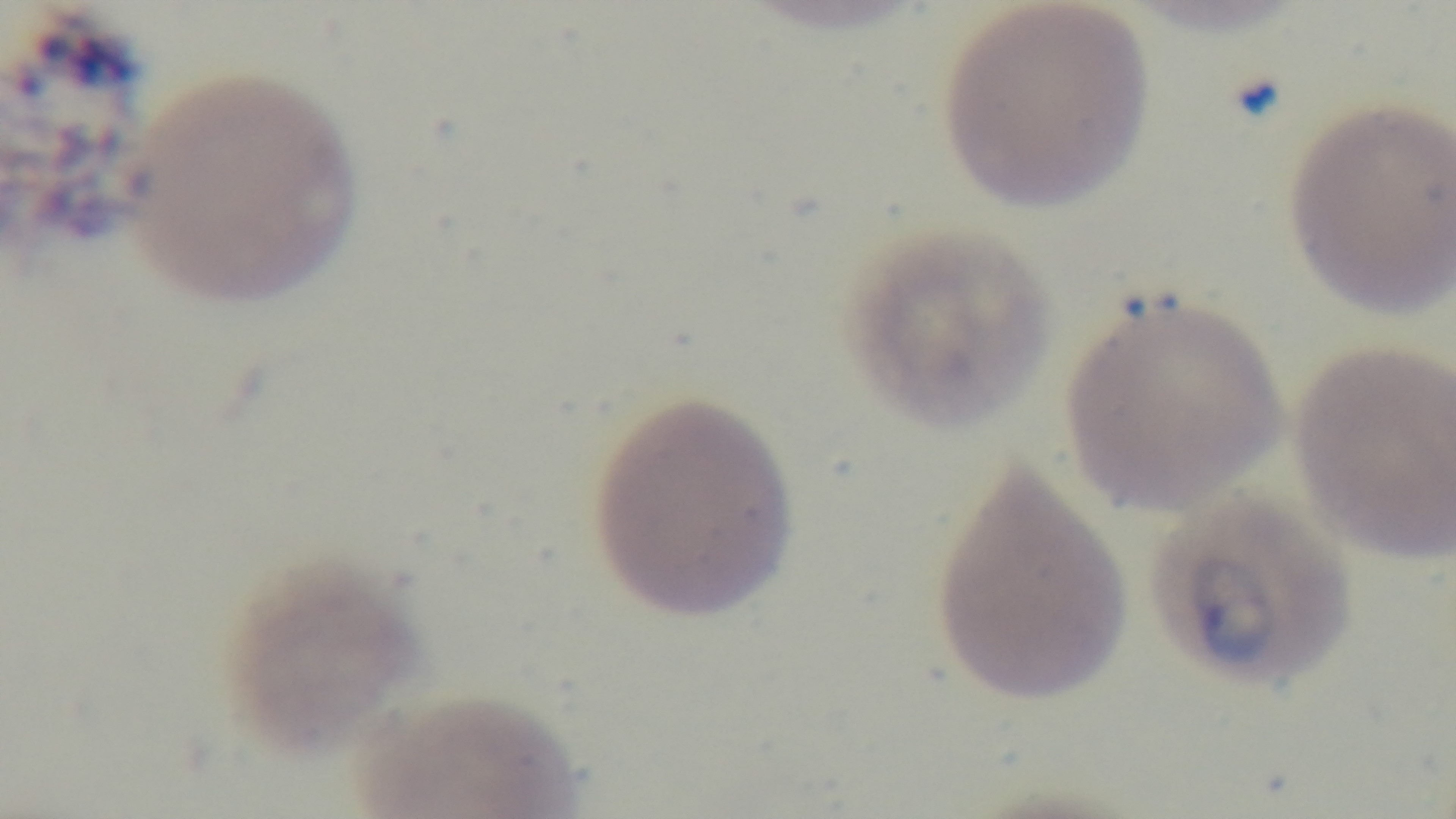
Summary:
  - Objective: 100x oil immersion
  - Modality: light microscopy
  - Stain: Giemsa
  - Field of view: one from the slide
  - Preparation: thin
  - Malaria status: infected
  - Capture: mounted 4K digital camera